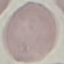

Result: no malaria parasites seen. Giemsa stain. Acquired by smartphone through the microscope eyepiece. Thin blood film. Cell patch, automatically extracted from a larger field of view and resized to 64 × 64 pixels.